Name the blood parasite species.
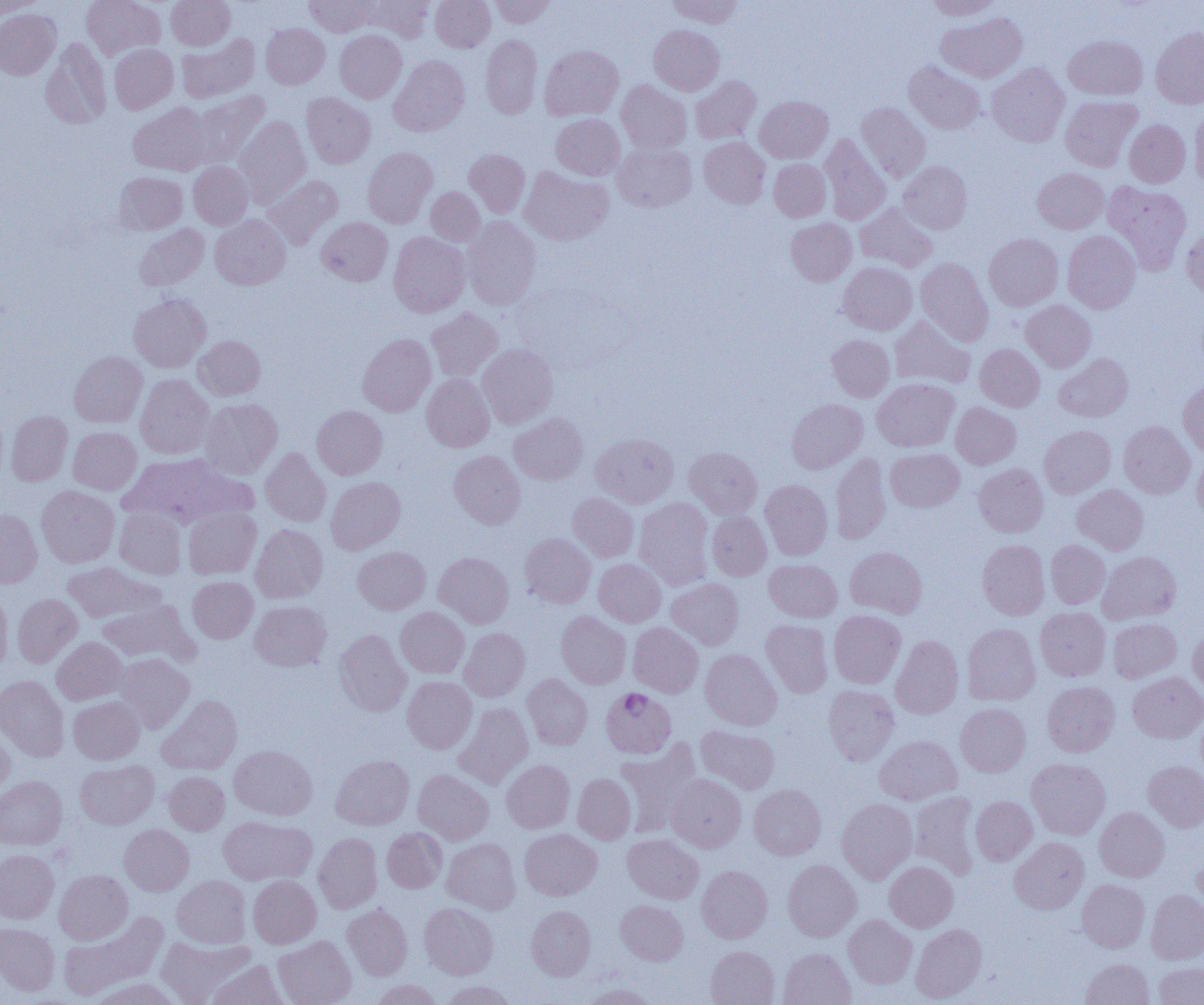
Plasmodium falciparum.

Approximate bounding boxes as (x1,y1)-(x2,y2) corner pairs in pixels. Plasmodium falciparum-infected red blood cell locations: (600,687)-(676,758). Uninfected red blood cell locations: (81,0)-(164,60), (166,0)-(235,50), (304,0)-(377,37), (362,0)-(434,43), (430,0)-(495,52), (489,0)-(555,28), (668,0)-(743,28), (924,0)-(1003,20), (0,1)-(44,19), (0,9)-(61,80), (937,12)-(1026,82), (261,23)-(330,89), (649,25)-(724,95), (1150,27)-(1204,108), (334,30)-(407,103), (177,33)-(259,102), (481,35)-(542,119), (1064,35)-(1147,100), (41,38)-(111,129), (109,44)-(178,113), (539,45)-(623,121), (389,56)-(470,136), (904,61)-(985,135), (987,62)-(1070,147), (690,76)-(761,145), (616,80)-(691,154), (191,91)-(269,167), (301,93)-(375,168), (755,95)-(833,163), (1060,96)-(1142,171), (129,102)-(212,176), (856,102)-(931,182), (1190,106)-(1204,190), (551,114)-(625,180), (234,115)-(311,207), (1124,119)-(1190,188), (820,135)-(891,225), (699,136)-(770,208), (613,143)-(696,212), (363,147)-(437,228), (464,149)-(530,217), (769,158)-(830,222), (899,160)-(972,234), (189,161)-(252,230), (520,167)-(613,245), (1032,168)-(1108,234), (114,172)-(187,235), (264,175)-(343,249), (1103,181)-(1192,274), (426,187)-(485,245), (855,203)-(936,272), (210,214)-(290,290), (317,217)-(392,286), (463,217)-(541,310), (786,218)-(857,286), (134,224)-(209,291), (1182,225)-(1204,300), (1063,230)-(1140,313), (388,232)-(470,317), (984,233)-(1063,311), (916,258)-(993,345), (838,262)-(917,335), (129,293)-(211,372), (1021,300)-(1096,372), (426,307)-(503,381), (890,315)-(976,390), (357,333)-(436,416), (827,335)-(894,402), (193,336)-(265,400), (478,344)-(558,429), (974,344)-(1045,411), (69,351)-(147,427), (1054,353)-(1133,422), (135,374)-(214,459), (422,374)-(494,451), (872,378)-(959,452), (1178,380)-(1204,457), (200,398)-(282,478), (787,398)-(867,474), (951,402)-(1020,469), (312,405)-(387,479), (6,411)-(73,486), (509,413)-(588,485), (1118,421)-(1196,499), (1039,425)-(1115,498), (68,427)-(141,495), (590,433)-(678,508), (684,447)-(762,518), (261,448)-(331,527), (885,448)-(964,512), (449,450)-(526,528), (1192,451)-(1204,521), (830,452)-(891,544), (119,453)-(251,527), (973,464)-(1048,537), (326,477)-(405,554), (760,480)-(833,560), (1072,484)-(1148,555), (37,485)-(120,568), (568,493)-(639,562), (634,497)-(714,589), (183,507)-(261,579), (114,508)-(186,578), (0,509)-(42,588), (707,510)-(771,580), (251,524)-(328,603), (520,533)-(595,608), (977,540)-(1049,620), (1046,540)-(1110,609), (353,546)-(430,614), (845,546)-(927,618), (1098,551)-(1181,624), (435,552)-(514,628), (594,559)-(666,627), (764,559)-(842,622), (62,562)-(162,623), (188,576)-(258,643), (666,578)-(744,650), (0,588)-(12,674), (12,593)-(82,668), (98,599)-(198,665), (250,601)-(331,671), (395,607)-(469,678), (1036,607)-(1110,681), (829,610)-(905,689), (556,611)-(631,689), (1108,618)-(1181,683), (760,619)-(833,698), (628,622)-(704,697), (962,622)-(1040,705), (459,627)-(530,701), (1188,627)-(1204,698), (334,629)-(411,716), (890,635)-(963,719), (52,637)-(129,705), (700,648)-(782,730), (115,653)-(194,732), (1128,672)-(1204,743), (523,674)-(592,750), (0,675)-(69,761), (402,676)-(476,753), (1042,681)-(1119,757), (823,685)-(899,765), (157,695)-(242,776), (68,696)-(145,764), (454,702)-(534,789), (955,703)-(1031,777), (1196,708)-(1204,783), (0,724)-(15,796), (696,724)-(779,794), (875,735)-(962,805), (616,741)-(702,837), (230,745)-(317,820), (331,754)-(414,830), (1027,758)-(1110,839), (501,759)-(574,833), (75,760)-(159,829), (1143,761)-(1204,832), (413,769)-(494,845), (164,772)-(229,835), (572,773)-(636,844), (667,774)-(746,852), (0,776)-(67,850), (749,784)-(826,860), (909,791)-(980,878), (970,796)-(1037,865), (837,798)-(917,884), (1094,807)-(1169,882), (218,816)-(316,885), (119,824)-(194,896), (382,827)-(447,893), (520,828)-(602,901), (313,832)-(382,914), (623,834)-(703,904), (1010,837)-(1089,914), (442,838)-(521,914), (0,849)-(59,924), (1192,851)-(1204,917), (783,859)-(861,941), (884,861)-(958,932), (696,864)-(772,943), (54,869)-(132,944), (171,875)-(251,948), (248,875)-(321,948), (1077,879)-(1150,953), (1145,889)-(1204,964), (616,900)-(688,966), (419,903)-(498,979), (342,904)-(412,980), (526,905)-(595,980), (58,912)-(168,1000), (843,914)-(917,988), (0,922)-(59,995), (910,924)-(986,1003), (273,935)-(356,1005), (156,936)-(254,1004), (705,945)-(779,1005), (778,948)-(855,1005), (1081,958)-(1154,1005), (206,959)-(289,1005), (1153,962)-(1204,1005), (86,977)-(184,1005), (370,979)-(443,1005), (440,980)-(518,1005), (579,983)-(659,1005). Thin blood film. One field of a larger specimen. 1000x magnification. Light microscopy. Image is 1204×1005 pixels.